Assess the morphology of the erythrocytes.
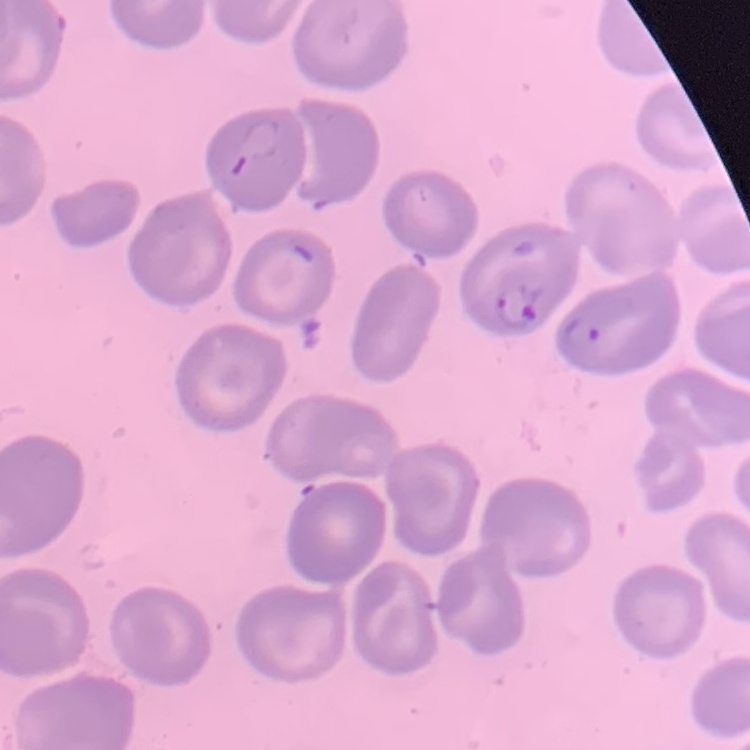

No rouleaux formation.

Thin blood film. Field's or Giemsa stain. One tile cut from a larger photomicrograph.